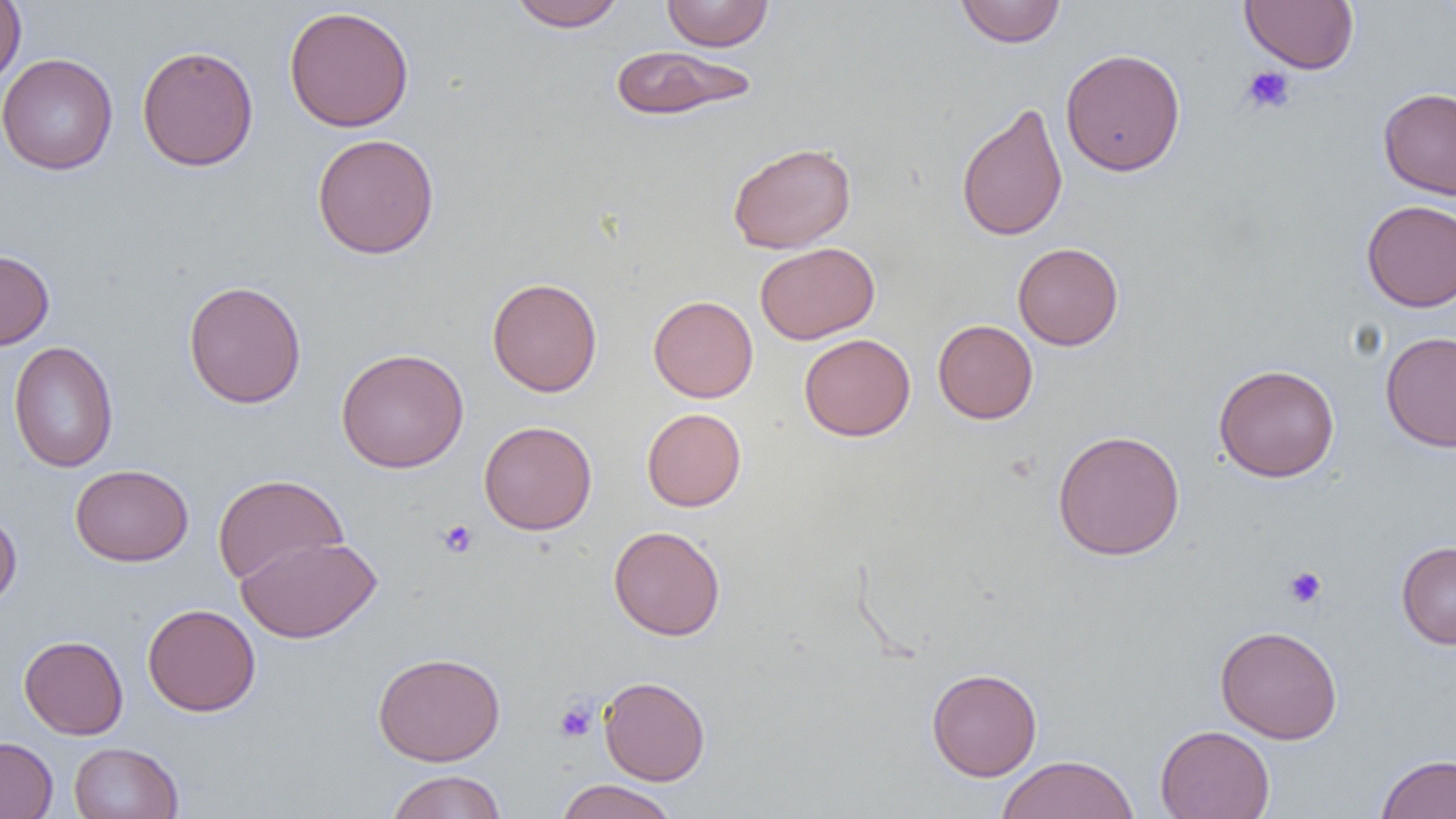
Approximate bounding boxes as [x1, y1, x2, y2] in pixels. Platelet locations: [1240, 66, 1295, 115], [437, 519, 478, 558], [1284, 566, 1327, 608], [554, 700, 598, 743]. Uninfected red blood cell locations: [0, 0, 26, 90], [507, 0, 626, 31], [661, 0, 775, 51], [955, 0, 1067, 47], [1240, 0, 1359, 74], [283, 5, 415, 132], [136, 44, 259, 172], [608, 44, 757, 121], [1060, 48, 1186, 176], [0, 53, 118, 176], [1378, 87, 1456, 200], [955, 101, 1068, 242], [312, 133, 440, 259], [727, 142, 857, 254], [1361, 199, 1456, 311], [755, 242, 880, 344], [1013, 242, 1124, 350], [0, 249, 55, 350], [487, 277, 602, 397], [183, 280, 307, 409], [648, 295, 758, 402], [933, 319, 1038, 424], [1380, 331, 1456, 452], [799, 333, 915, 441], [8, 341, 119, 474], [336, 348, 469, 473], [1213, 363, 1340, 483], [641, 408, 747, 512], [478, 420, 598, 535], [1052, 429, 1185, 560], [70, 464, 194, 567], [212, 474, 348, 586], [0, 505, 22, 612], [608, 525, 726, 641], [237, 535, 381, 643], [1396, 541, 1456, 650], [142, 603, 261, 716], [1215, 625, 1343, 743], [18, 635, 128, 739], [373, 651, 506, 766], [926, 667, 1042, 781], [599, 675, 711, 786], [1155, 724, 1275, 819], [0, 735, 58, 818], [68, 741, 183, 819], [1376, 753, 1456, 818], [997, 754, 1140, 819], [385, 770, 507, 819], [555, 779, 680, 819]. Slide-level diagnosis: no evidence of blood parasites. Thin blood film. Image is 1456×819 pixels. 1000x magnification. Single field of view. Optical microscopy.